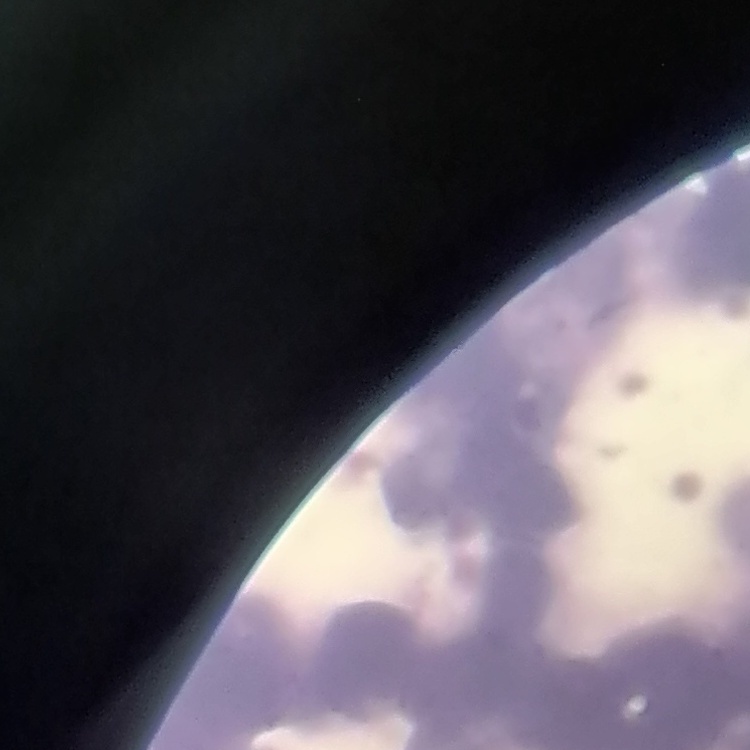

red_blood_cell_morphology: rouleaux formation
stain: Field's or Giemsa
preparation: thin blood film
image_type: square crop of a larger photomicrograph